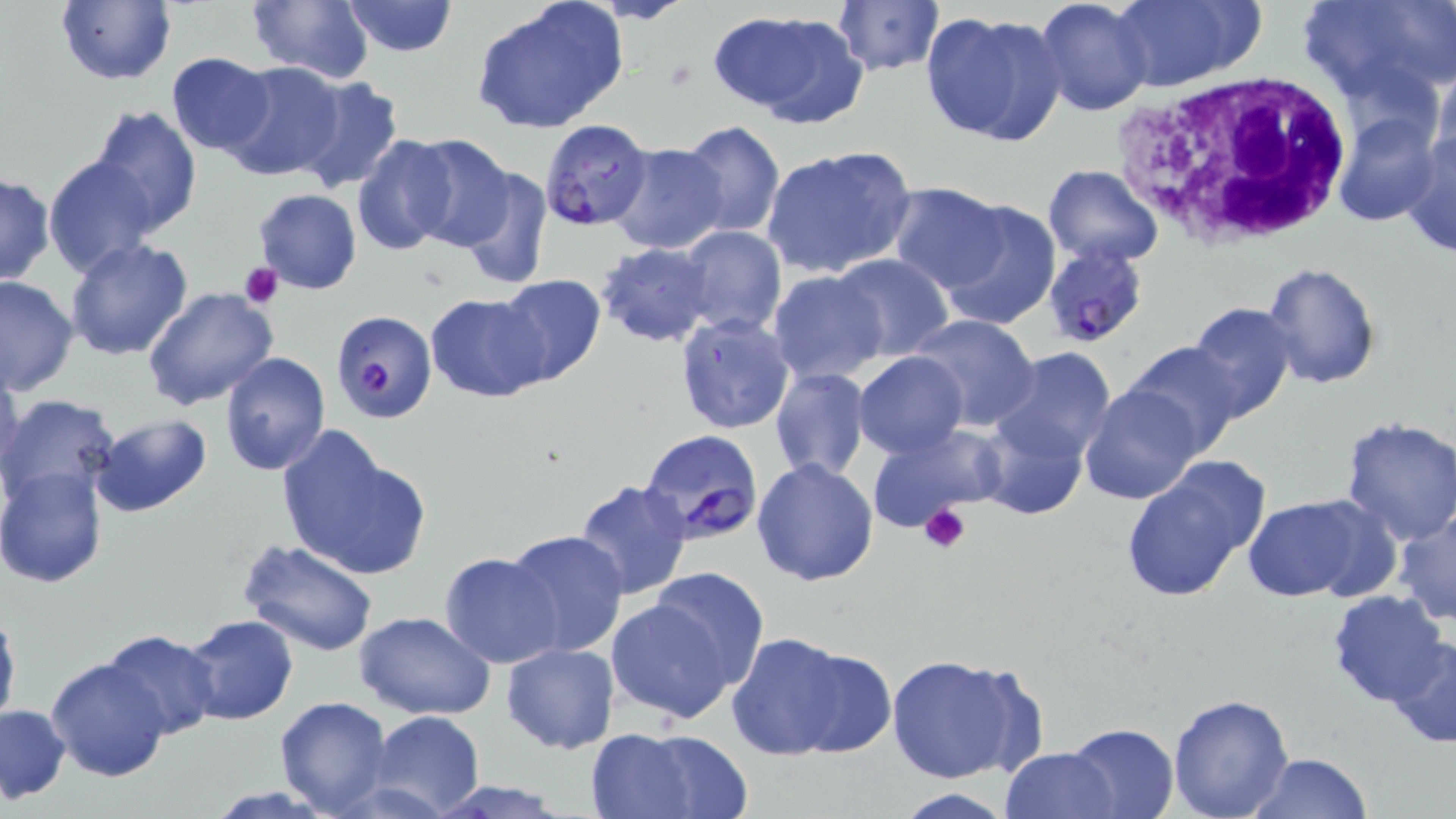

slide-level diagnosis = Plasmodium falciparum
preparation = thin blood film
image size = 1456×819 pixels
stain = May-Grünwald-Giemsa
white blood cell locations = approximate bounding boxes as [x1, y1, x2, y2] in pixels: [1106, 70, 1356, 247]
field of view = one of a larger specimen
Plasmodium falciparum-infected red blood cell locations = approximate bounding boxes as [x1, y1, x2, y2] in pixels: [539, 120, 653, 230], [1043, 246, 1150, 346], [332, 309, 437, 424], [641, 428, 765, 543]
modality = light microscopy
magnification = 1000x
platelet locations = approximate bounding boxes as [x1, y1, x2, y2] in pixels: [237, 262, 283, 310], [917, 501, 971, 554]
uninfected red blood cell locations = approximate bounding boxes as [x1, y1, x2, y2] in pixels: [471, 0, 629, 134], [1032, 0, 1156, 117], [1108, 0, 1262, 90], [1298, 0, 1455, 103], [55, 1, 175, 85], [244, 1, 375, 83], [340, 1, 459, 56], [831, 2, 945, 78], [714, 9, 869, 127], [921, 9, 1067, 148], [166, 52, 277, 156], [221, 62, 346, 183], [1432, 63, 1456, 174], [290, 75, 405, 196], [88, 105, 203, 234], [1335, 113, 1441, 226], [679, 121, 785, 238], [1400, 126, 1456, 259], [404, 133, 519, 250], [351, 135, 461, 254], [608, 143, 729, 255], [761, 143, 916, 278], [44, 155, 161, 278], [1042, 164, 1163, 267], [456, 165, 552, 290], [0, 172, 54, 286], [886, 182, 1011, 292], [252, 189, 362, 294], [935, 196, 1061, 331], [679, 226, 786, 337], [64, 237, 193, 360], [595, 243, 716, 348], [832, 255, 956, 362], [1262, 262, 1381, 388], [769, 270, 889, 383], [495, 274, 607, 389], [0, 275, 79, 398], [142, 286, 279, 411], [426, 293, 550, 402], [1187, 302, 1298, 425], [675, 312, 797, 435], [909, 313, 1041, 431], [1121, 342, 1245, 457], [987, 346, 1117, 467], [220, 351, 330, 475], [854, 351, 968, 458], [0, 366, 25, 489], [769, 367, 871, 484], [1078, 385, 1206, 505], [0, 394, 126, 513], [975, 408, 1089, 519], [90, 415, 214, 518], [1339, 417, 1456, 543], [863, 423, 1008, 533], [276, 427, 431, 581], [1117, 457, 1271, 604], [752, 458, 880, 586], [0, 464, 109, 588], [573, 479, 694, 602], [1245, 495, 1384, 603], [1393, 507, 1456, 626], [504, 529, 628, 656], [238, 537, 380, 655], [438, 552, 564, 669], [647, 567, 770, 692], [1327, 591, 1451, 709], [603, 594, 746, 724], [0, 601, 20, 736], [352, 610, 495, 719], [181, 614, 298, 725], [101, 629, 221, 740], [727, 633, 885, 761], [1386, 638, 1456, 747], [501, 642, 619, 753], [883, 654, 1042, 787], [46, 656, 171, 782], [1166, 694, 1295, 819], [274, 696, 391, 816], [0, 703, 71, 804], [368, 710, 485, 817], [1063, 722, 1180, 819], [592, 728, 753, 818], [999, 746, 1122, 819], [1246, 753, 1372, 819], [422, 780, 579, 818], [890, 789, 1020, 819]